Identify the parasite.
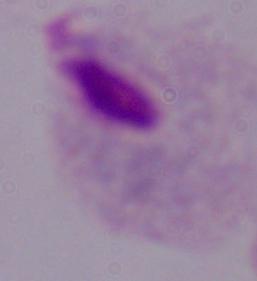

A trichomonad.

1000x magnification. Micrograph.